Locate every blood parasite and identify its species.
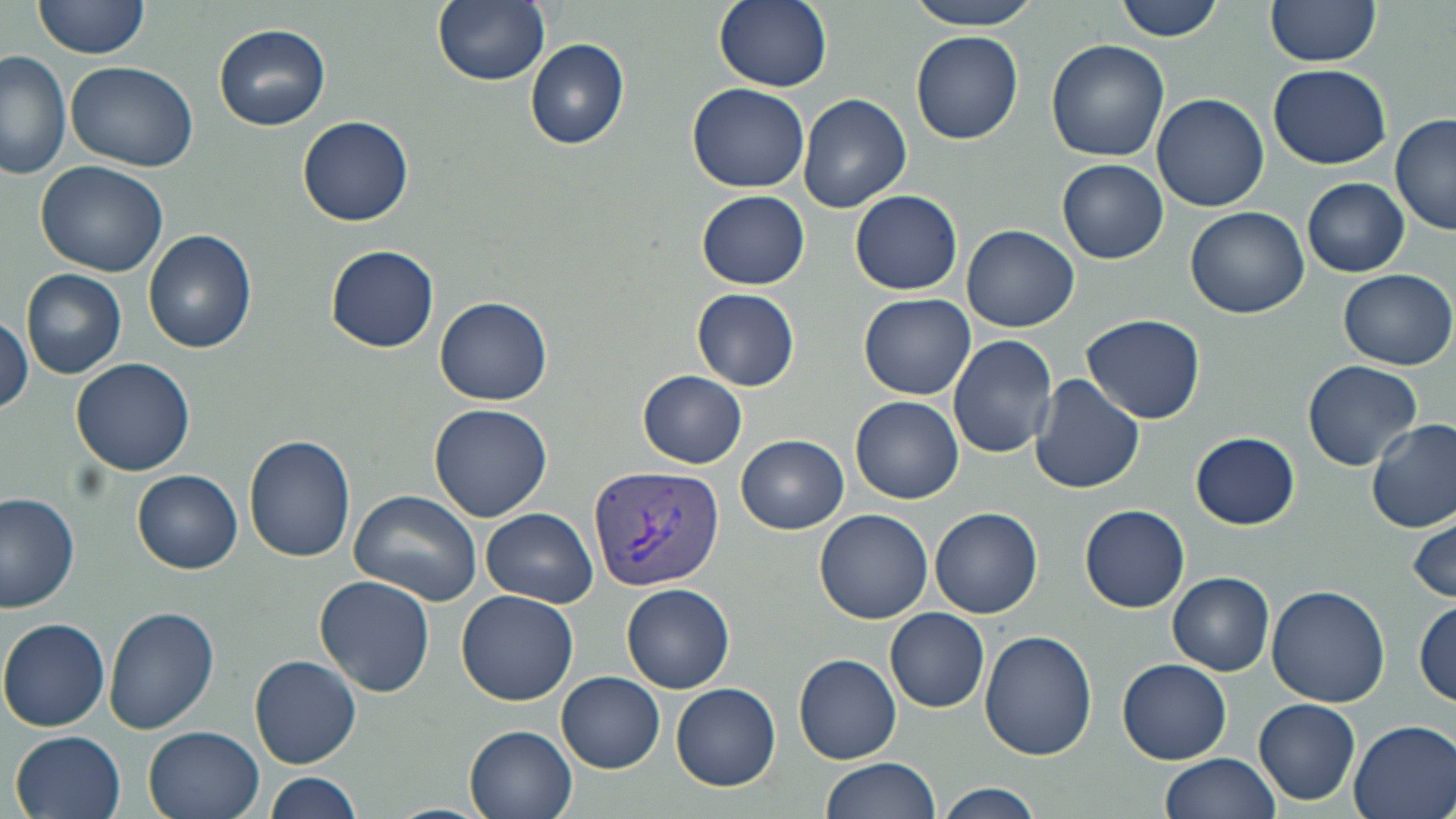
Approximate bounding boxes as (x1, y1, x2, y2) in pixels.
Plasmodium vivax-infected red blood cells: (587, 462, 725, 592).
No Plasmodium falciparum, Plasmodium ovale, Plasmodium malariae, Babesia divergens, or Trypanosoma brucei observed.

slide-level diagnosis = Plasmodium vivax
image size = 1456×819 pixels
stain = May-Grünwald-Giemsa
preparation = thin blood film
modality = light microscopy
field of view = single
uninfected red blood cell locations = approximate bounding boxes as (x1, y1, x2, y2) in pixels: (33, 0, 150, 58), (433, 0, 549, 87), (712, 0, 832, 92), (899, 0, 1049, 29), (1114, 0, 1226, 43), (1264, 1, 1379, 69), (214, 24, 331, 130), (912, 30, 1024, 144), (526, 38, 630, 149), (1045, 40, 1170, 162), (0, 50, 73, 181), (66, 60, 200, 169), (1268, 64, 1391, 169), (687, 83, 809, 193), (1152, 92, 1269, 211), (798, 94, 912, 211), (1390, 114, 1455, 237), (297, 115, 413, 226), (1058, 159, 1167, 264), (37, 160, 169, 276), (1302, 177, 1409, 276), (850, 189, 963, 295), (698, 190, 810, 289), (1185, 206, 1309, 319), (962, 223, 1079, 332), (145, 231, 258, 355), (326, 246, 439, 352), (22, 269, 127, 379), (1337, 269, 1455, 369), (692, 289, 800, 391), (859, 293, 976, 399), (435, 296, 553, 405), (1082, 313, 1205, 423), (0, 315, 32, 415), (948, 335, 1058, 459), (72, 358, 195, 475), (1302, 360, 1423, 471), (1328, 367, 1448, 524), (636, 369, 748, 468), (1030, 373, 1144, 495), (851, 396, 962, 503), (429, 403, 551, 521), (1367, 418, 1456, 533), (1189, 432, 1301, 530), (243, 433, 356, 562), (736, 434, 848, 533), (134, 471, 242, 574), (350, 490, 483, 605), (0, 493, 79, 612), (1079, 503, 1191, 613), (930, 506, 1043, 618), (482, 509, 597, 605), (814, 509, 934, 625), (1409, 513, 1455, 604), (1167, 573, 1275, 675), (313, 575, 434, 695), (621, 582, 735, 694), (1266, 585, 1390, 707), (456, 590, 580, 706), (1414, 598, 1455, 704), (105, 605, 217, 733), (885, 607, 990, 712), (0, 618, 112, 731), (981, 630, 1099, 762), (793, 653, 901, 764), (250, 655, 360, 767), (1116, 658, 1231, 762), (557, 671, 664, 773), (671, 683, 781, 790), (1254, 698, 1360, 805), (1348, 719, 1456, 819), (464, 723, 578, 819), (144, 725, 265, 819), (11, 730, 127, 819), (1159, 752, 1282, 818), (823, 756, 943, 818), (263, 772, 364, 818), (934, 782, 1043, 819)
magnification = 1000x